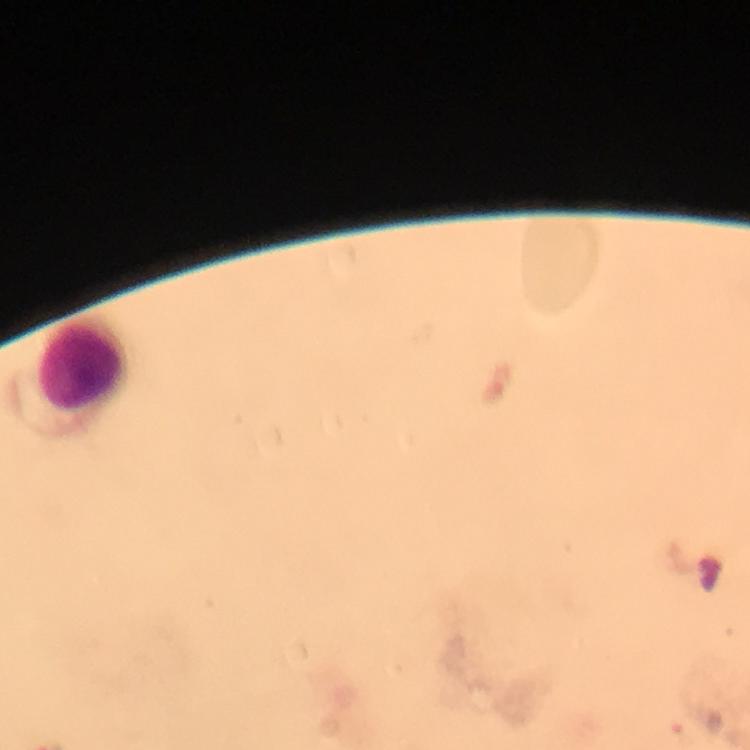
Approximate centers as {x, y} in pixels.
Summary:
  - Leukocyte locations: {83, 365}
  - Plasmodium parasites: none detected
  - Preparation: thick blood smear
  - Context: from a malaria diagnostic workup
  - Stain: Giemsa
  - Image size: 750×750 pixels
  - Capture: smartphone photograph through a microscope
  - Cropped from: one field of view
  - Immersion oil: used
  - Magnification: 100x